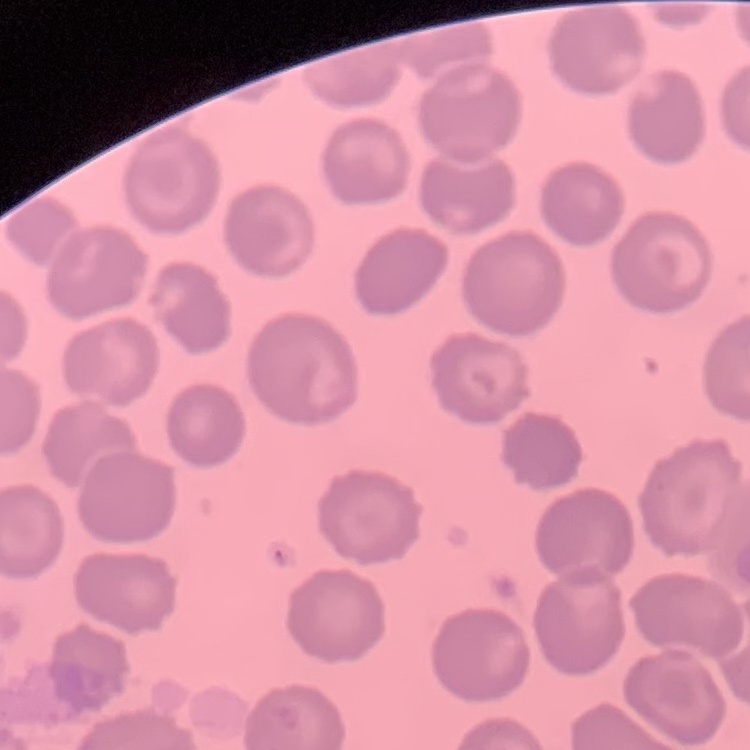 The red blood cells exhibit no rouleaux formation. Thin blood film. Stained with either Field's or Giemsa. One tile cut from a larger photomicrograph.